Point out each Plasmodium parasite and each leukocyte.
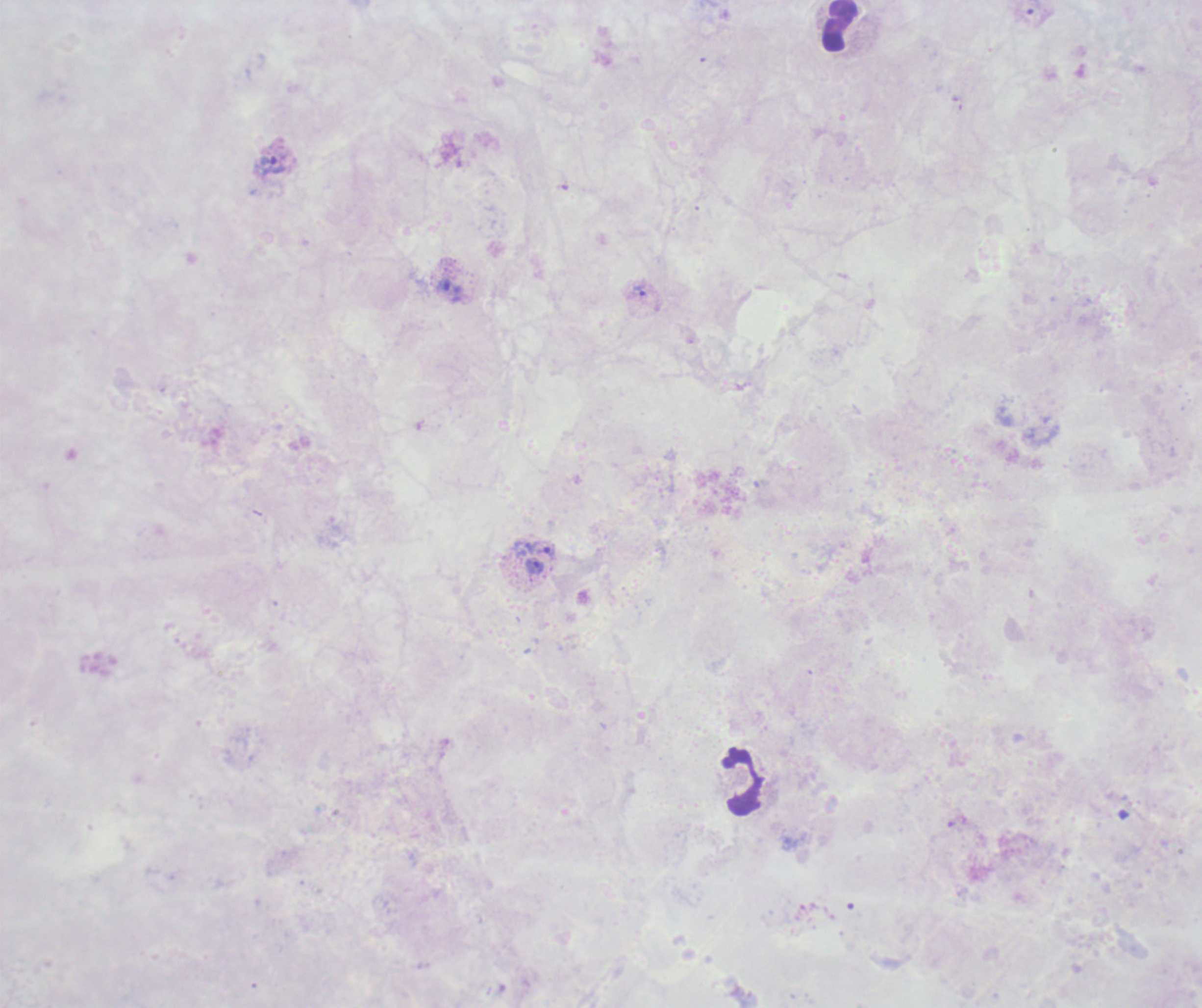
Approximate object centers, in pixels from the top-left corner.
Trophozoites: (x=269, y=165), (x=450, y=291), (x=639, y=291), (x=548, y=551), (x=536, y=566).
No schizont or gametocyte forms observed.
Leukocytes: (x=840, y=25), (x=742, y=782).

context = previously used in a real diagnosis
preparation = thick blood film
magnification = 100x
image size = 1202×1008 pixels
field of view = one from this slide
background quality = unsatisfactory
coloration quality = bad
stain = Romanowsky